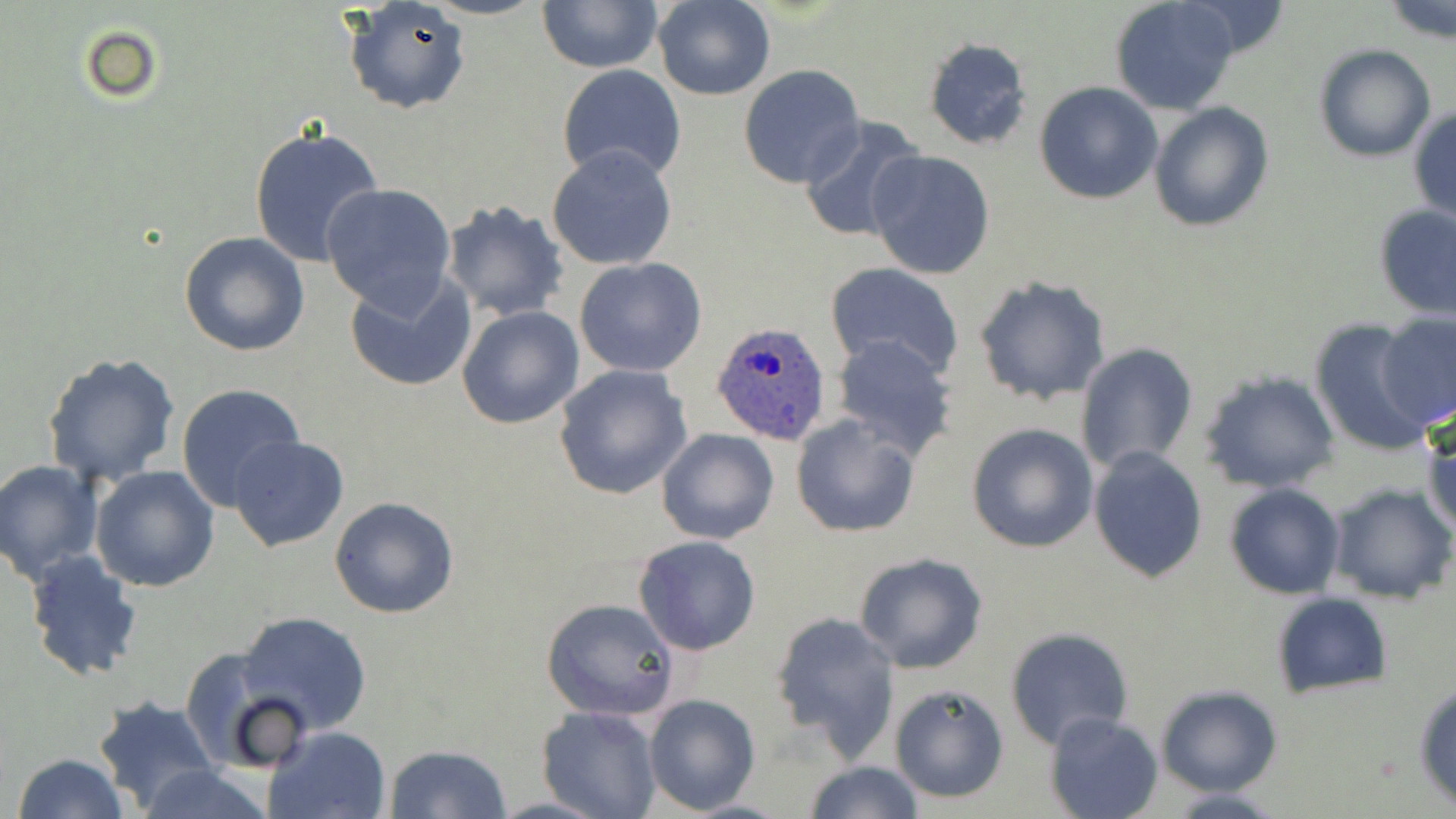

slide-level diagnosis = Plasmodium ovale
uninfected red blood cell locations = approximate bounding boxes as (x1, y1, x2, y2) in pixels: (424, 0, 546, 21), (537, 0, 662, 72), (652, 0, 776, 101), (1180, 0, 1291, 60), (342, 1, 469, 116), (1110, 2, 1241, 116), (1383, 2, 1456, 45), (922, 36, 1031, 151), (1314, 45, 1437, 162), (556, 65, 689, 186), (737, 65, 867, 190), (1033, 81, 1163, 204), (1149, 101, 1274, 231), (1409, 104, 1456, 225), (798, 115, 927, 243), (249, 123, 385, 267), (547, 143, 678, 269), (866, 150, 996, 281), (320, 183, 456, 314), (438, 199, 569, 321), (1373, 204, 1456, 320), (179, 231, 311, 358), (574, 257, 707, 378), (826, 262, 964, 380), (343, 270, 476, 392), (973, 276, 1112, 406), (456, 306, 583, 429), (1375, 311, 1456, 428), (1306, 317, 1435, 455), (832, 335, 959, 458), (1075, 342, 1200, 473), (42, 350, 181, 488), (552, 365, 694, 502), (1197, 369, 1341, 495), (176, 382, 306, 510), (790, 413, 920, 537), (1423, 416, 1456, 538), (966, 422, 1098, 553), (657, 428, 779, 546), (227, 436, 350, 553), (1088, 447, 1209, 583), (1, 460, 102, 582), (91, 466, 220, 591), (1325, 482, 1455, 605), (1225, 484, 1345, 599), (329, 496, 460, 620), (633, 535, 762, 656), (23, 548, 143, 684), (853, 552, 989, 674), (1270, 591, 1392, 701), (541, 597, 679, 722), (769, 610, 902, 760), (238, 612, 373, 737), (1005, 628, 1134, 751), (182, 650, 308, 775), (1413, 678, 1456, 811), (1154, 683, 1283, 797), (890, 684, 1010, 803), (643, 693, 760, 812), (92, 696, 219, 816), (537, 706, 660, 819), (1045, 710, 1162, 818), (265, 726, 390, 819), (385, 742, 513, 819), (12, 753, 126, 819), (804, 761, 926, 818), (134, 762, 271, 819), (1159, 787, 1296, 819)
modality = light microscopy
image size = 1456×819 pixels
stain = May-Grünwald-Giemsa
magnification = 1000x
Plasmodium ovale-infected red blood cell locations = approximate bounding boxes as (x1, y1, x2, y2) in pixels: (712, 323, 832, 445)
preparation = thin blood smear
field of view = one of a larger specimen